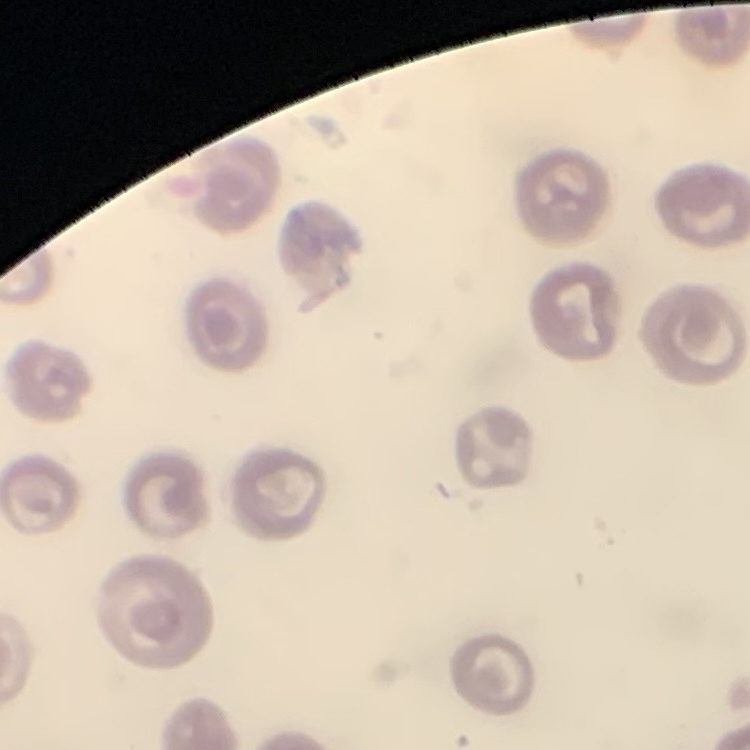

The red blood cells show no rouleaux formation. Thin blood smear. One tile cut from a larger photomicrograph. Stained with either Field's or Giemsa.